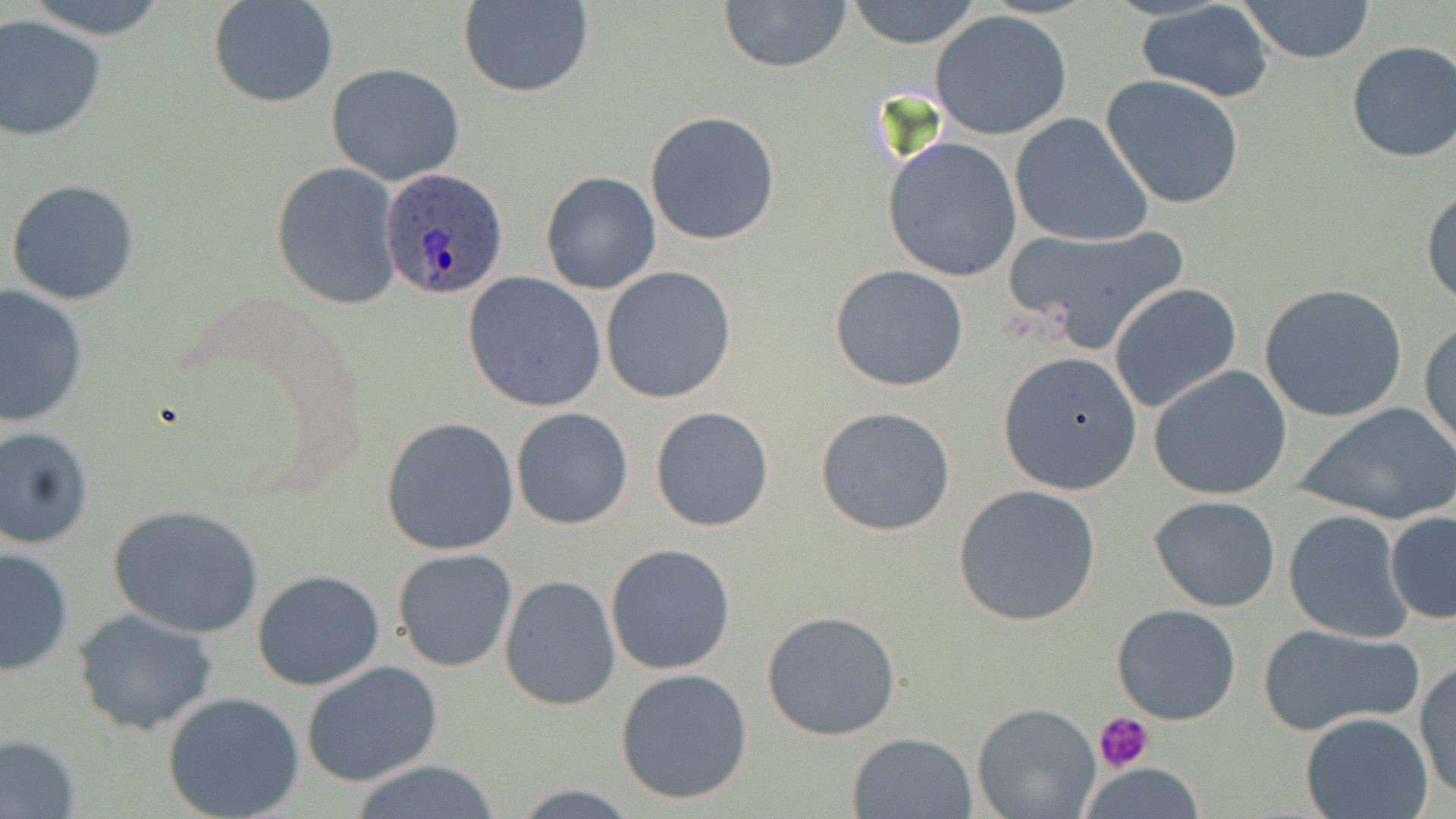

Summary:
  - Coordinate format: approximate bounding boxes as (x1,y1)-(x2,y2) corner pairs in pixels
  - Plasmodium ovale-infected red blood cell locations: (379,167)-(510,299)
  - Uninfected red blood cell locations: (17,0)-(176,39), (209,0)-(339,107), (718,0)-(854,72), (843,0)-(984,49), (1232,0)-(1377,64), (460,1)-(593,98), (1134,1)-(1278,104), (929,10)-(1073,141), (0,18)-(107,142), (1345,40)-(1456,164), (326,62)-(466,186), (1100,74)-(1246,210), (645,111)-(783,246), (1009,112)-(1156,248), (882,136)-(1023,281), (271,163)-(400,308), (540,171)-(661,295), (6,179)-(140,304), (1421,181)-(1456,310), (1003,225)-(1187,352), (830,264)-(969,391), (600,266)-(736,404), (463,271)-(606,413), (1109,283)-(1241,412), (1258,284)-(1408,423), (1,286)-(89,427), (1420,319)-(1455,458), (999,352)-(1141,493), (1149,365)-(1294,500), (1291,401)-(1455,526), (650,406)-(776,532), (815,406)-(955,535), (511,408)-(634,529), (381,416)-(519,555), (0,426)-(95,549), (953,484)-(1103,627), (1149,495)-(1281,612), (107,504)-(266,637), (1384,509)-(1456,624), (1282,511)-(1414,643), (606,544)-(736,675), (1,545)-(74,676), (393,549)-(517,672), (252,569)-(386,691), (501,577)-(619,710), (1112,603)-(1241,725), (71,607)-(223,737), (761,610)-(900,741), (1258,622)-(1425,737), (1414,659)-(1455,803), (301,661)-(443,787), (615,668)-(753,805), (162,691)-(304,818), (973,702)-(1102,819), (1301,712)-(1435,819), (847,731)-(978,819), (0,733)-(82,819), (343,760)-(510,818), (1074,762)-(1207,818), (507,784)-(641,817)
  - Platelet locations: (1096,712)-(1154,774)
  - Slide-level diagnosis: Plasmodium ovale
  - Modality: optical microscopy
  - Field of view: single
  - Image size: 1456×819 pixels
  - Magnification: 1000x
  - Preparation: thin blood smear
  - Stain: May-Grünwald-Giemsa